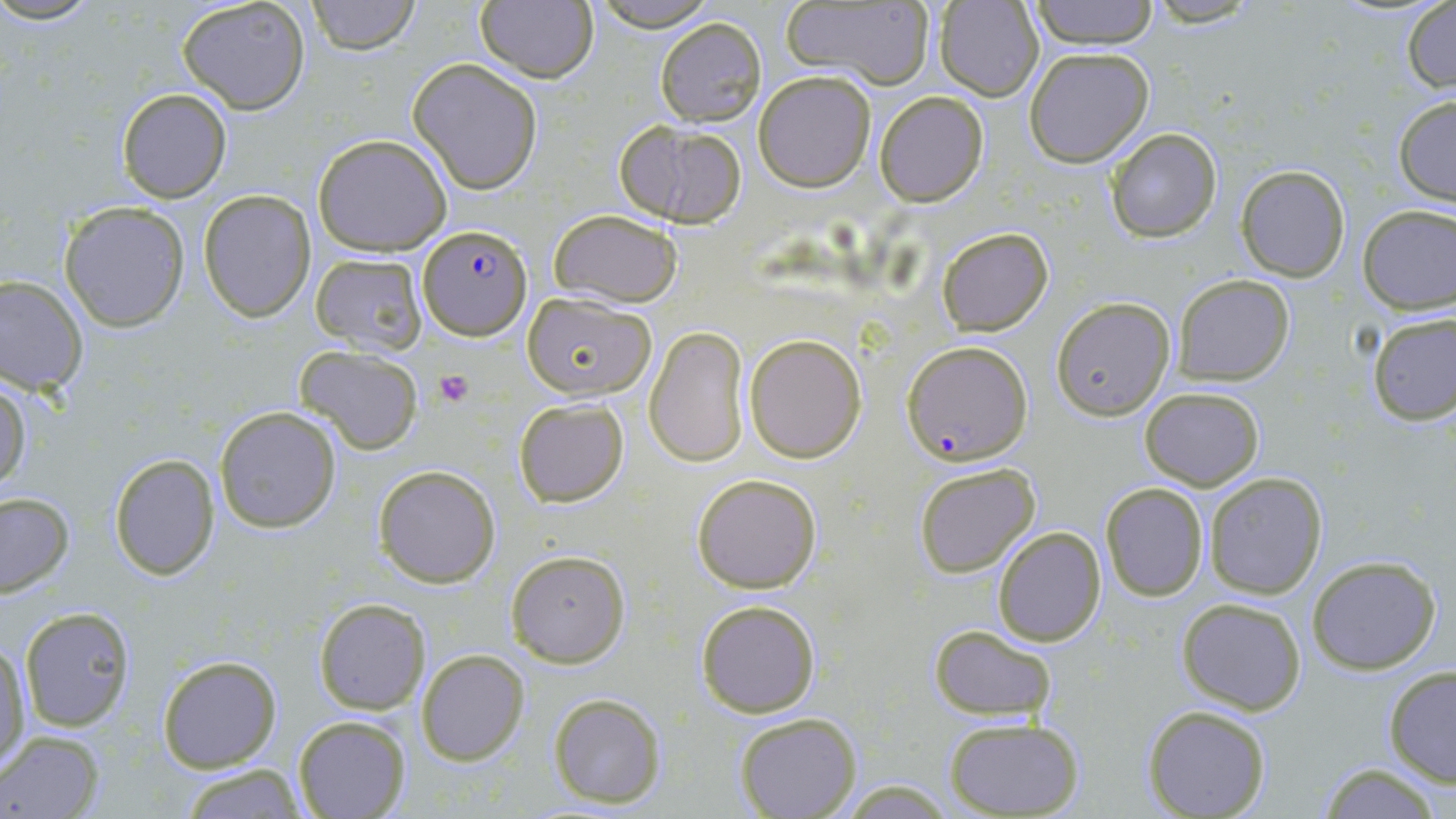
Summary:
  - Coordinate format: approximate bounding boxes as (x1, y1, x2, y2) in pixels
  - Uninfected red blood cell locations: (0, 0, 106, 26), (177, 0, 311, 114), (308, 0, 418, 54), (475, 0, 597, 83), (590, 0, 720, 30), (1028, 0, 1160, 49), (1142, 0, 1267, 28), (779, 1, 935, 88), (935, 1, 1045, 101), (1402, 2, 1456, 93), (654, 17, 767, 126), (1024, 47, 1153, 168), (407, 59, 543, 193), (752, 70, 875, 191), (115, 88, 232, 203), (874, 92, 989, 207), (1393, 97, 1456, 206), (615, 119, 749, 229), (1103, 128, 1222, 243), (313, 133, 452, 256), (1236, 166, 1351, 282), (199, 189, 315, 322), (60, 202, 189, 331), (1357, 204, 1456, 313), (546, 208, 685, 309), (936, 227, 1053, 335), (309, 252, 429, 356), (0, 274, 87, 394), (1171, 275, 1295, 386), (522, 292, 657, 399), (1051, 297, 1178, 421), (1366, 311, 1454, 426), (645, 325, 751, 470), (745, 334, 865, 463), (294, 345, 423, 454), (0, 379, 31, 496), (1140, 388, 1265, 491), (513, 398, 629, 507), (215, 406, 342, 532), (109, 454, 221, 580), (912, 462, 1041, 578), (373, 464, 500, 587), (691, 473, 822, 594), (1203, 473, 1328, 600), (1100, 482, 1209, 602), (0, 492, 75, 598), (991, 528, 1105, 646), (506, 550, 630, 667), (1305, 555, 1440, 675), (1177, 598, 1307, 715), (314, 599, 429, 715), (694, 600, 820, 717), (18, 605, 137, 730), (928, 624, 1056, 721), (1, 640, 30, 771), (417, 649, 529, 765), (156, 655, 282, 772), (1383, 666, 1456, 785), (546, 692, 667, 808), (1142, 705, 1271, 818), (733, 712, 862, 819), (294, 715, 412, 819), (943, 717, 1086, 818), (1, 730, 104, 817), (1317, 763, 1447, 819), (175, 765, 308, 817)
  - Platelet locations: (432, 370, 474, 408)
  - Plasmodium falciparum-infected red blood cell locations: (417, 222, 533, 340), (906, 342, 1034, 465)
  - Slide-level diagnosis: Plasmodium falciparum
  - Stain: May-Grünwald-Giemsa
  - Preparation: thin blood film
  - Magnification: 1000x
  - Modality: light microscopy
  - Field of view: single
  - Image size: 1456×819 pixels